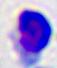
Captured at 400x magnification. Micrograph. A leukocyte is seen.